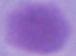

Summary:
  - Modality: micrograph
  - Identification: erythrocyte
  - Magnification: 1000x